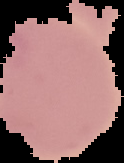 From a thin blood smear. Segmented cell region on a black background. Malaria status: uninfected. Image is 124×163 pixels.